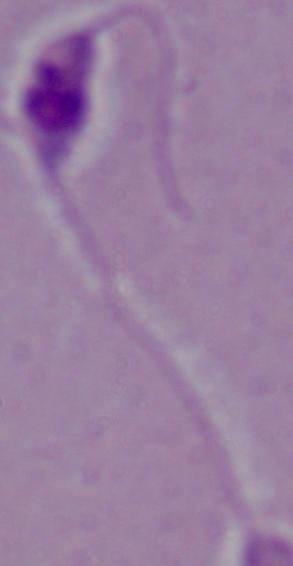

Summary:
  - Magnification: 1000x
  - Identification: Leishmania
  - Modality: photomicrograph